Assess this cell for malaria.
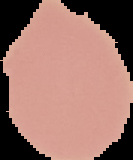

Uninfected.

The area outside the segmented cell region is set to black. Image is 133×160 pixels. From a thin blood film.